Comment on the morphology of the red blood cells.
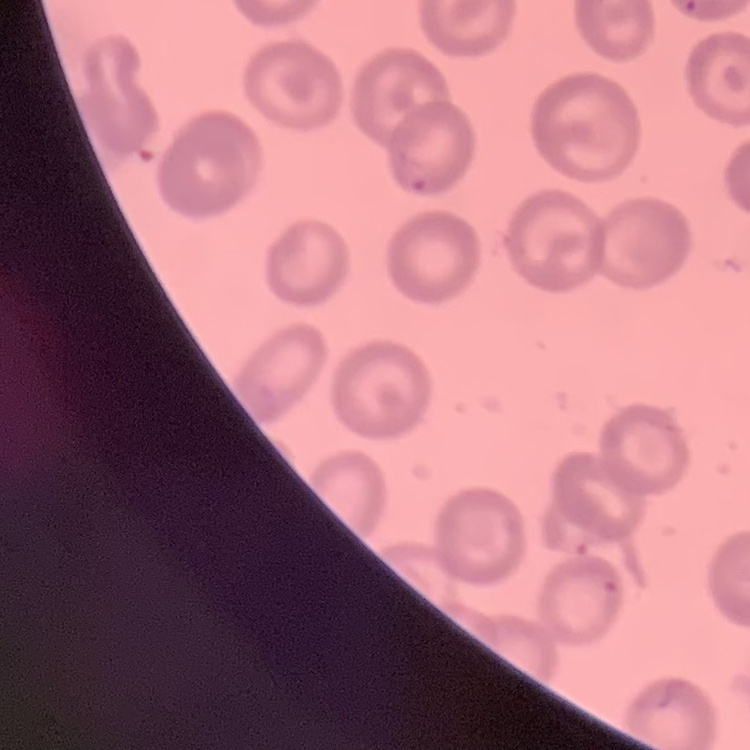

No rouleaux formation.

Thin peripheral smear. Square crop of a larger photomicrograph. Field's or Giemsa stain.